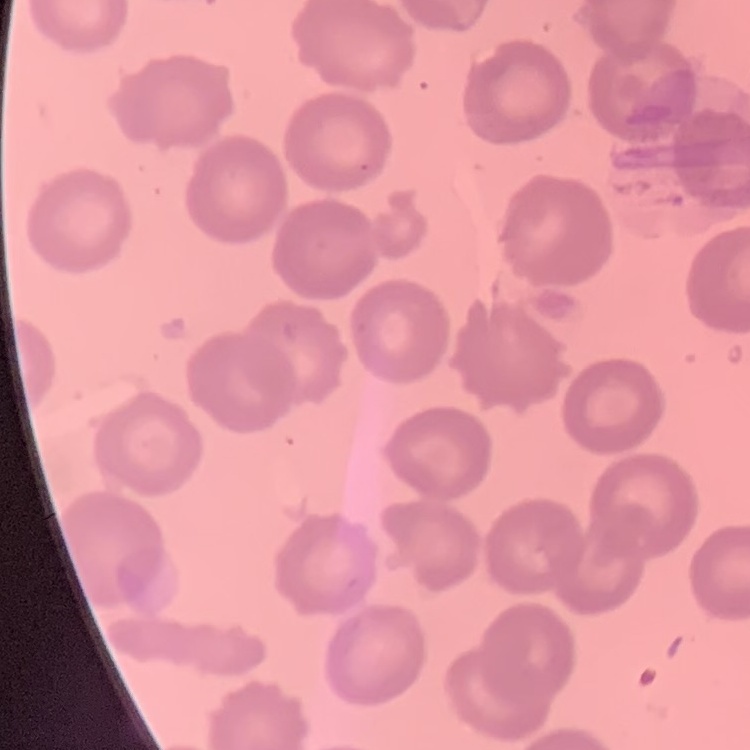

Summary:
  - Erythrocyte morphology: no rouleaux formation
  - Image type: square crop of a larger photomicrograph
  - Preparation: thin blood film
  - Stain: Field's or Giemsa